Report the malaria status of this cell.
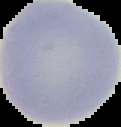

Uninfected.

Image is 121×127 pixels. From a thin blood film. Cell region segmented out of the field of view; the surrounding area is masked to black.